Assess the morphology of the red blood cells.
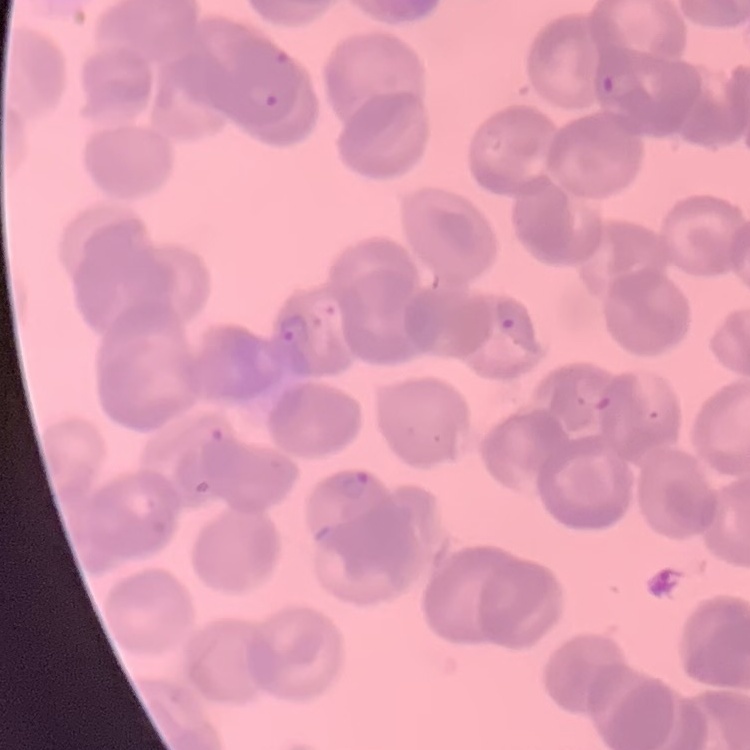
Rouleaux formation.

Summary:
  - Stain: Field's or Giemsa
  - Preparation: thin blood film
  - Image type: one tile cut from a larger photomicrograph